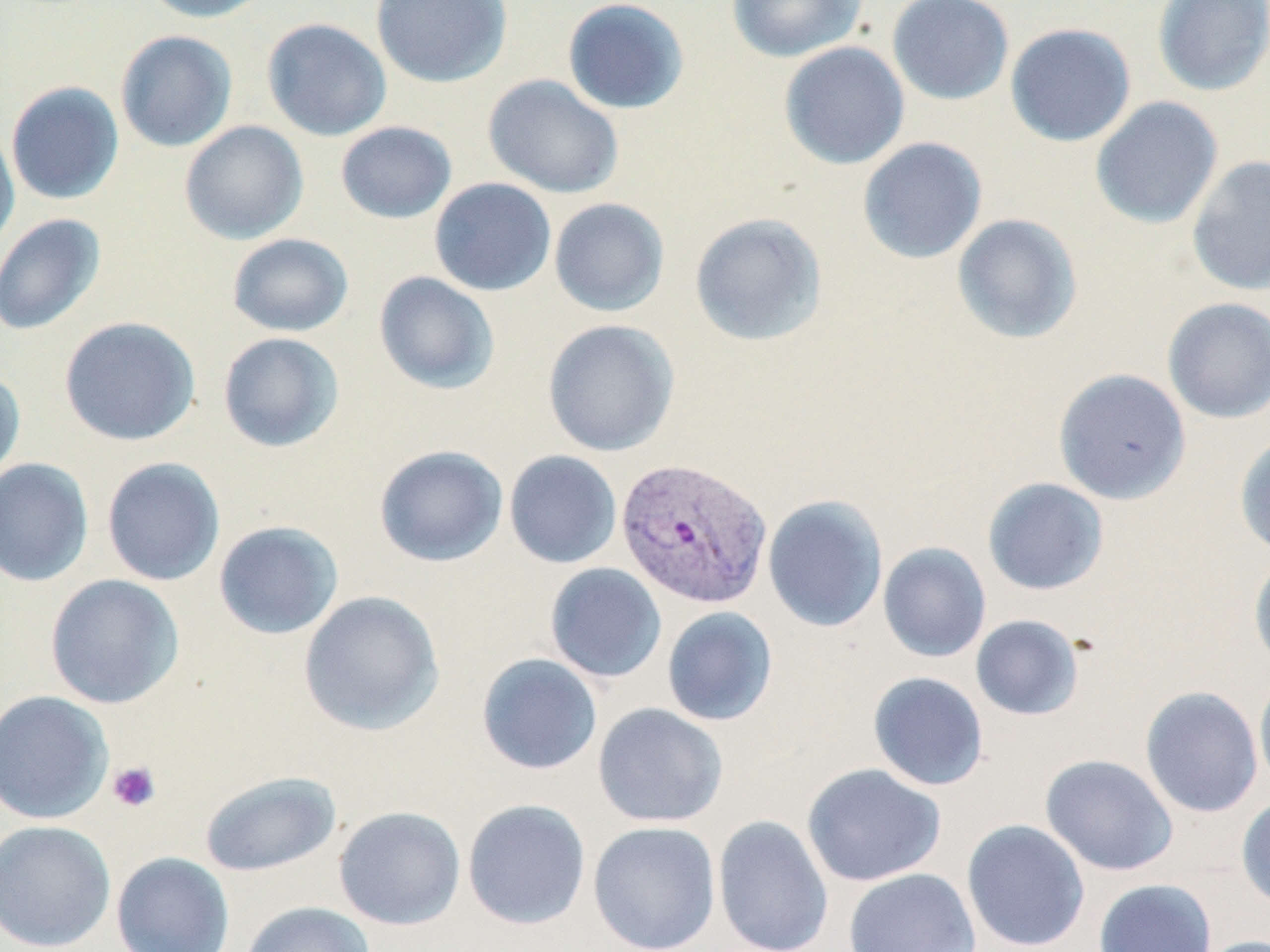

Summary:
  - Coordinate format: approximate bounding boxes as (x1, y1, x2, y2) in pixels
  - Plasmodium vivax-infected red blood cell locations: (615, 456, 773, 609)
  - Platelet locations: (106, 760, 162, 813)
  - Uninfected red blood cell locations: (138, 0, 273, 23), (371, 0, 513, 88), (726, 0, 867, 63), (886, 0, 1015, 106), (1152, 0, 1270, 97), (562, 1, 690, 114), (261, 18, 392, 142), (1004, 22, 1137, 147), (115, 30, 238, 153), (779, 41, 910, 170), (483, 74, 625, 199), (6, 82, 125, 205), (1090, 96, 1224, 230), (179, 121, 309, 245), (336, 121, 457, 224), (0, 122, 19, 253), (857, 137, 988, 265), (1186, 155, 1270, 296), (429, 177, 557, 296), (548, 198, 670, 317), (689, 212, 827, 347), (0, 213, 106, 336), (952, 213, 1083, 345), (227, 233, 353, 337), (374, 272, 499, 395), (1162, 297, 1270, 424), (59, 316, 201, 446), (542, 319, 680, 457), (217, 332, 344, 452), (0, 367, 26, 483), (1053, 368, 1191, 505), (1234, 434, 1270, 558), (374, 445, 508, 568), (503, 450, 622, 569), (101, 456, 226, 586), (0, 457, 94, 587), (982, 477, 1109, 596), (762, 495, 888, 632), (213, 521, 344, 640), (878, 542, 991, 662), (1248, 553, 1270, 672), (544, 563, 667, 683), (45, 574, 185, 709), (298, 590, 444, 736), (661, 606, 779, 727), (970, 614, 1085, 721), (476, 653, 603, 775), (867, 671, 989, 791), (1254, 673, 1270, 793), (1139, 686, 1264, 818), (0, 690, 113, 825), (592, 702, 729, 828), (1040, 754, 1178, 876), (801, 763, 947, 887), (200, 771, 341, 877), (1236, 795, 1270, 911), (462, 798, 591, 930), (333, 806, 466, 930), (713, 814, 834, 952), (0, 819, 116, 952), (961, 819, 1091, 951), (587, 821, 721, 951), (111, 851, 235, 952), (843, 868, 982, 952), (1093, 878, 1217, 952), (241, 901, 376, 952), (1196, 935, 1270, 952)
  - Slide-level diagnosis: Plasmodium vivax
  - Modality: light microscopy
  - Stain: May-Grünwald-Giemsa
  - Field of view: one of a larger specimen
  - Image size: 1270×952 pixels
  - Preparation: thin blood smear
  - Magnification: 1000x